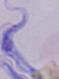
magnification = 1000x
identification = trypanosome
modality = micrograph